Identify the parasite.
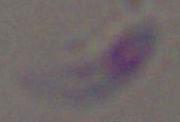
This is Toxoplasma gondii.

Summary:
  - Modality: photomicrograph
  - Magnification: 1000x